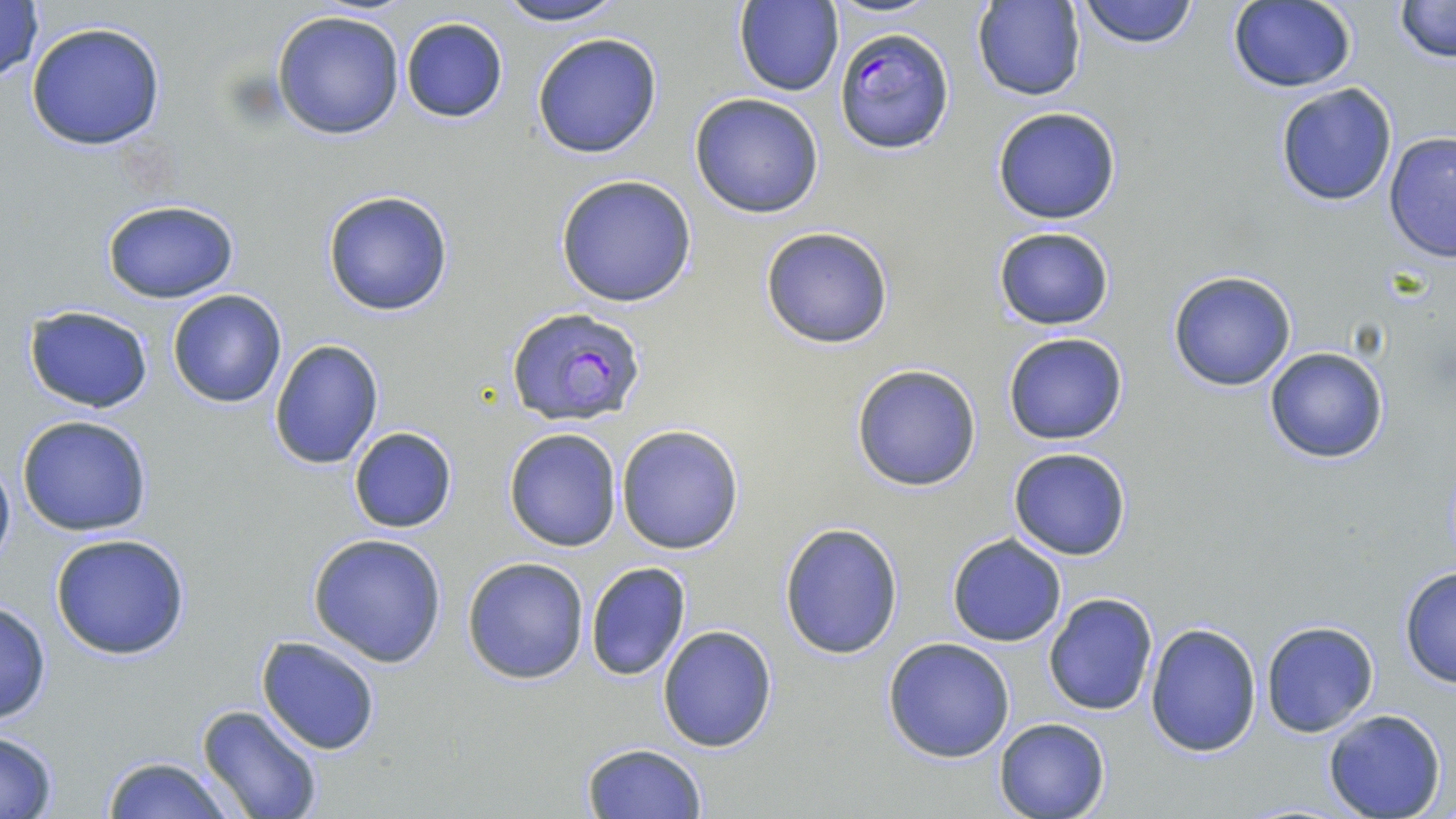

Approximate bounding boxes as (x1, y1, x2, y2) in pixels. Plasmodium falciparum-infected red blood cell locations: (834, 28, 954, 156), (506, 305, 646, 424). Uninfected red blood cell locations: (0, 0, 45, 84), (490, 0, 631, 27), (1075, 0, 1201, 50), (1391, 0, 1455, 66), (973, 1, 1087, 102), (1225, 1, 1358, 92), (734, 2, 843, 97), (271, 9, 406, 141), (399, 17, 508, 124), (24, 21, 168, 151), (530, 32, 663, 159), (1274, 82, 1397, 207), (689, 91, 826, 219), (990, 105, 1122, 225), (1384, 130, 1456, 264), (555, 173, 697, 307), (322, 190, 454, 317), (98, 199, 241, 303), (759, 226, 895, 348), (992, 226, 1117, 330), (1167, 270, 1297, 392), (167, 289, 287, 408), (25, 307, 153, 413), (1002, 332, 1129, 445), (268, 338, 383, 470), (1263, 347, 1388, 463), (850, 363, 983, 492), (17, 414, 154, 536), (616, 424, 746, 556), (348, 426, 458, 534), (503, 426, 623, 551), (1008, 447, 1132, 561), (0, 454, 15, 572), (778, 521, 905, 658), (49, 532, 193, 660), (308, 532, 449, 668), (946, 534, 1067, 647), (462, 556, 591, 684), (584, 562, 692, 681), (1398, 565, 1456, 688), (1043, 594, 1159, 716), (0, 597, 52, 726), (1261, 620, 1380, 737), (1146, 621, 1262, 759), (657, 625, 778, 751), (257, 636, 381, 755), (882, 636, 1015, 763), (197, 703, 326, 819), (1321, 709, 1447, 819), (993, 717, 1109, 819), (0, 731, 60, 816), (582, 742, 707, 818), (98, 754, 236, 819). Slide-level diagnosis: Plasmodium falciparum. One field of a larger specimen. Optical microscopy. May-Grünwald-Giemsa stain. Image is 1456×819 pixels. Thin blood smear. Captured at 1000x magnification.